Identify the parasite.
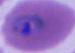

This is Plasmodium.

Captured at either 400x or 1000x magnification. Micrograph.